Assess for Plasmodium parasites.
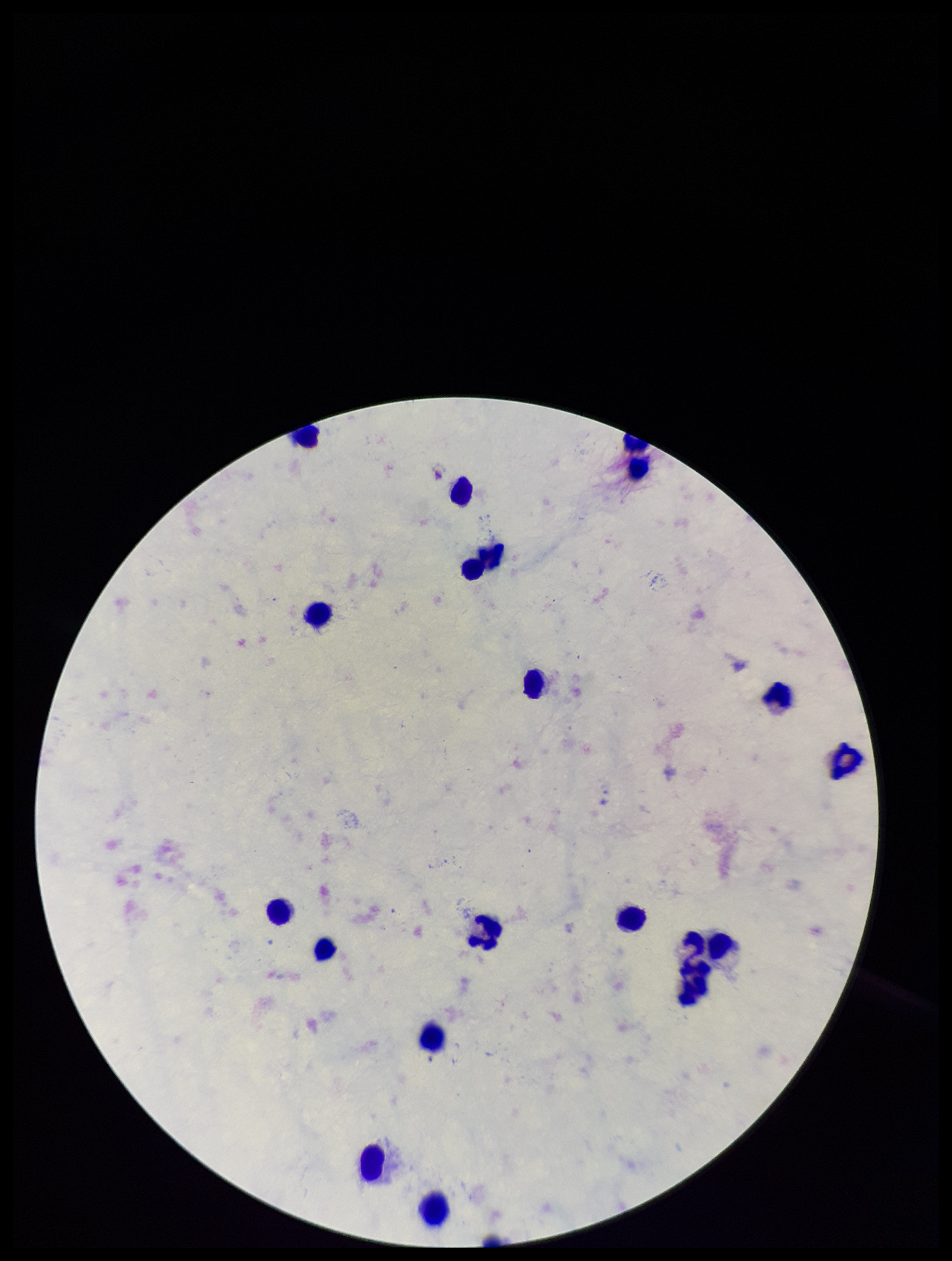

None detected.

One field from this slide. Leukocyte count: 19. Image is 952×1261 pixels. Preparation: thick smear. Photographed through the microscope eyepiece with a smartphone camera. Giemsa stain. Parasite count: 0. Species reported for this patient: Plasmodium falciparum. Patient malaria status: infected.